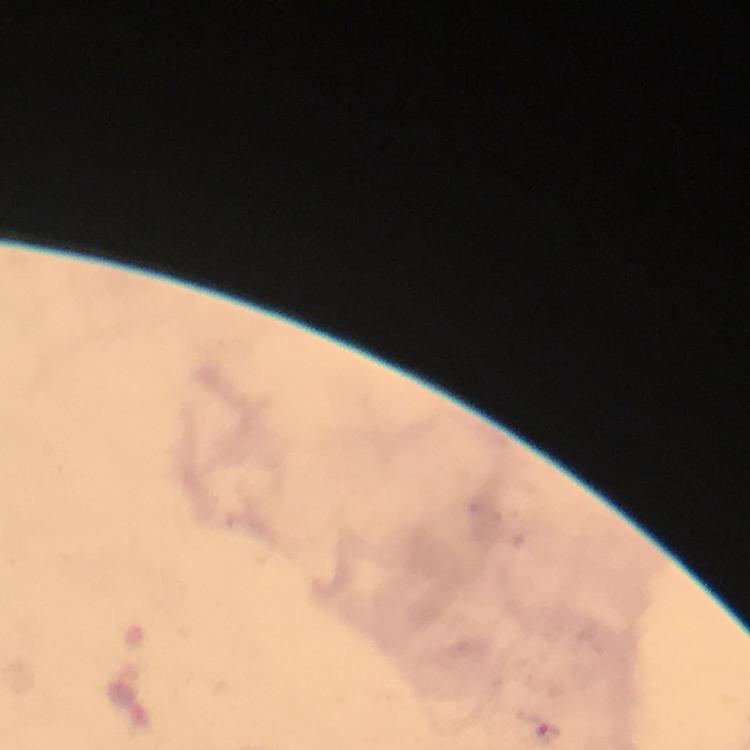

Approximate centers as {x, y} in pixels.
Summary:
  - Malaria parasite locations: {549, 730}
  - Cropped from: a single field of view
  - Magnification: 100x
  - Capture: smartphone mounted on the microscope
  - Immersion oil: applied
  - Context: from a malaria diagnostic workup
  - Stain: Giemsa
  - Image size: 750×750 pixels
  - Preparation: thick blood film